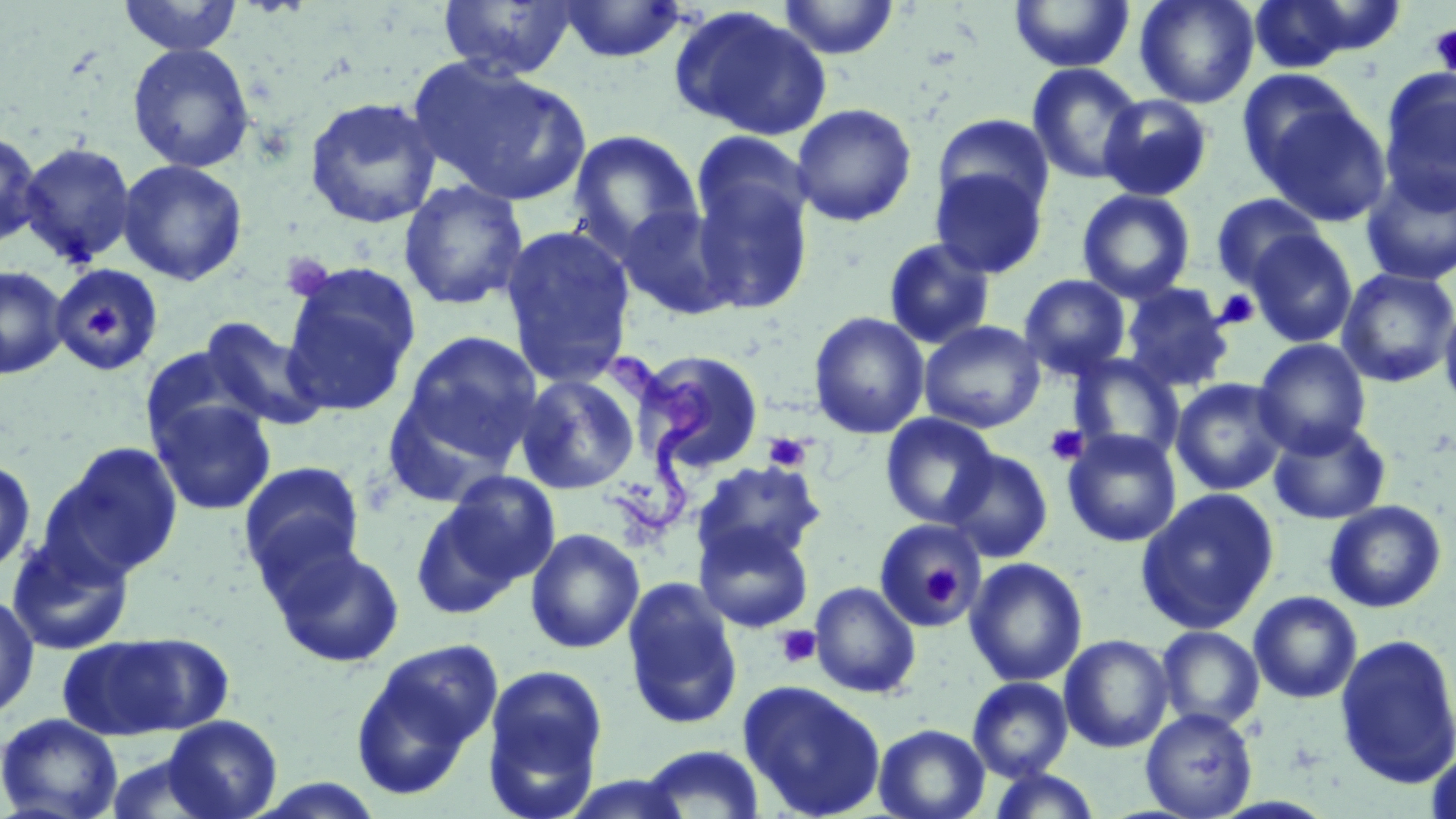
Summary:
  - Coordinate format: approximate bounding boxes as (x1,y1)-(x2,y2) corner pairs in pixels
  - Uninfected red blood cell locations: (437,0)-(576,80), (557,0)-(688,63), (777,0)-(899,60), (1009,0)-(1134,72), (1135,0)-(1259,109), (1245,0)-(1373,73), (118,1)-(243,57), (669,6)-(832,141), (127,43)-(256,173), (411,59)-(592,206), (1027,62)-(1145,184), (1379,67)-(1456,209), (1236,68)-(1364,187), (1098,94)-(1213,201), (303,95)-(443,229), (1257,98)-(1392,226), (791,103)-(917,227), (932,113)-(1055,220), (0,128)-(42,250), (567,129)-(704,260), (690,131)-(814,250), (18,141)-(136,266), (117,159)-(248,286), (930,167)-(1048,278), (1360,167)-(1456,286), (690,168)-(815,314), (398,179)-(529,311), (1076,188)-(1196,303), (1210,193)-(1327,291), (616,204)-(736,320), (500,224)-(636,388), (1246,229)-(1358,348), (882,237)-(996,350), (281,262)-(421,415), (52,264)-(164,374), (0,265)-(69,379), (1337,267)-(1456,387), (1018,274)-(1131,380), (1121,283)-(1234,392), (1439,299)-(1456,415), (808,311)-(930,439), (199,317)-(326,432), (919,320)-(1045,433), (398,329)-(544,468), (1253,338)-(1371,457), (139,346)-(263,451), (636,349)-(765,474), (1070,354)-(1183,461), (515,373)-(641,495), (1170,378)-(1290,496), (148,396)-(277,516), (879,413)-(1000,527), (1268,418)-(1391,525), (1063,429)-(1182,547), (43,441)-(184,580), (943,442)-(1179,554), (942,448)-(1053,563), (0,458)-(37,577), (238,460)-(366,588), (692,460)-(825,568), (431,471)-(561,598), (1136,488)-(1280,634), (1323,500)-(1447,613), (874,519)-(988,632), (695,522)-(813,633), (525,528)-(644,654), (5,533)-(135,656), (269,542)-(406,668), (964,557)-(1088,687), (621,577)-(744,731), (809,581)-(921,698), (0,591)-(39,721), (1248,591)-(1363,703), (1156,625)-(1265,731), (58,631)-(224,741), (1059,633)-(1174,753), (1334,633)-(1456,790), (349,640)-(503,798), (481,662)-(609,817), (967,676)-(1073,781), (738,680)-(887,819), (1140,707)-(1257,818), (0,712)-(123,819), (160,715)-(283,819), (873,723)-(990,819), (640,745)-(766,818), (1424,745)-(1456,819), (987,767)-(1102,818), (559,773)-(693,818)
  - Trypanosoma brucei locations: (586,347)-(720,535)
  - Platelet locations: (1429,24)-(1456,78), (280,253)-(335,301), (1214,289)-(1260,330), (87,300)-(120,339), (1045,424)-(1089,465), (763,432)-(811,471), (922,566)-(959,609), (775,625)-(821,669)
  - Slide-level diagnosis: Trypanosoma brucei
  - Magnification: 1000x
  - Image size: 1456×819 pixels
  - Modality: light microscopy
  - Stain: May-Grünwald-Giemsa
  - Field of view: one of a larger specimen
  - Preparation: thin blood film